State which parasite is depicted.
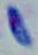
This is Toxoplasma gondii.

Summary:
  - Magnification: 1000x
  - Modality: micrograph